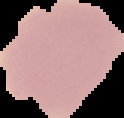

preparation = thin blood smear
image size = 124×118 pixels
image type = cell region segmented out of the field of view; surrounding area masked to black
malaria status = uninfected